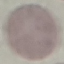
Result: no malaria parasites detected. Thin blood smear. Giemsa-stained preparation. Cell patch, automatically extracted from a larger field of view and resized to 64 × 64 pixels. Acquired by smartphone through the microscope eyepiece.